Assess the morphology of the erythrocytes.
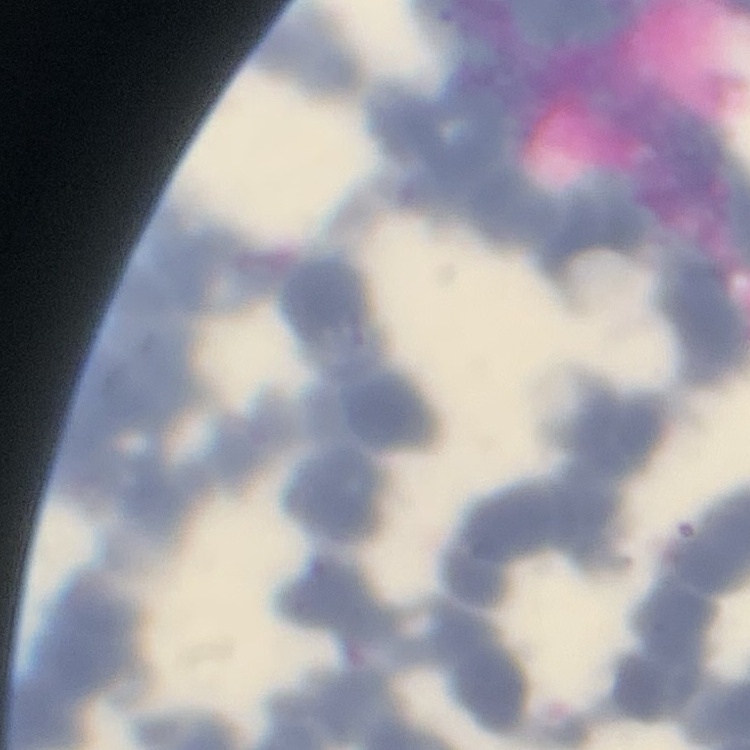

Rouleaux formation.

Summary:
  - Stain: Field's or Giemsa
  - Image type: square crop of a larger photomicrograph
  - Preparation: thin blood film